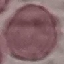
Malaria status: uninfected. Cell patch, automatically extracted from a larger field of view and resized to 64 × 64 pixels. Giemsa stain. Photographed with a smartphone camera at the microscope eyepiece. Thin blood film.